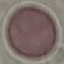
Result: no malaria parasites detected. Thin blood film. Giemsa-stained preparation. Cell patch, automatically extracted from a larger field of view and resized to 64 × 64 pixels. Photographed with a smartphone camera at the microscope eyepiece.